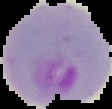

Image is 112×109 pixels. Segmented cell region on a black background. Result: Plasmodium parasites identified. From a thin blood smear.